State which parasite is depicted.
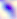
This is Toxoplasma gondii.

magnification: 400x
modality: micrograph